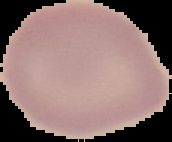
Summary:
  - Image size: 172×142 pixels
  - Preparation: thin blood smear
  - Image type: cell region segmented out of the field of view; surrounding area masked to black
  - Result: negative for malaria parasites